Name the blood parasite species.
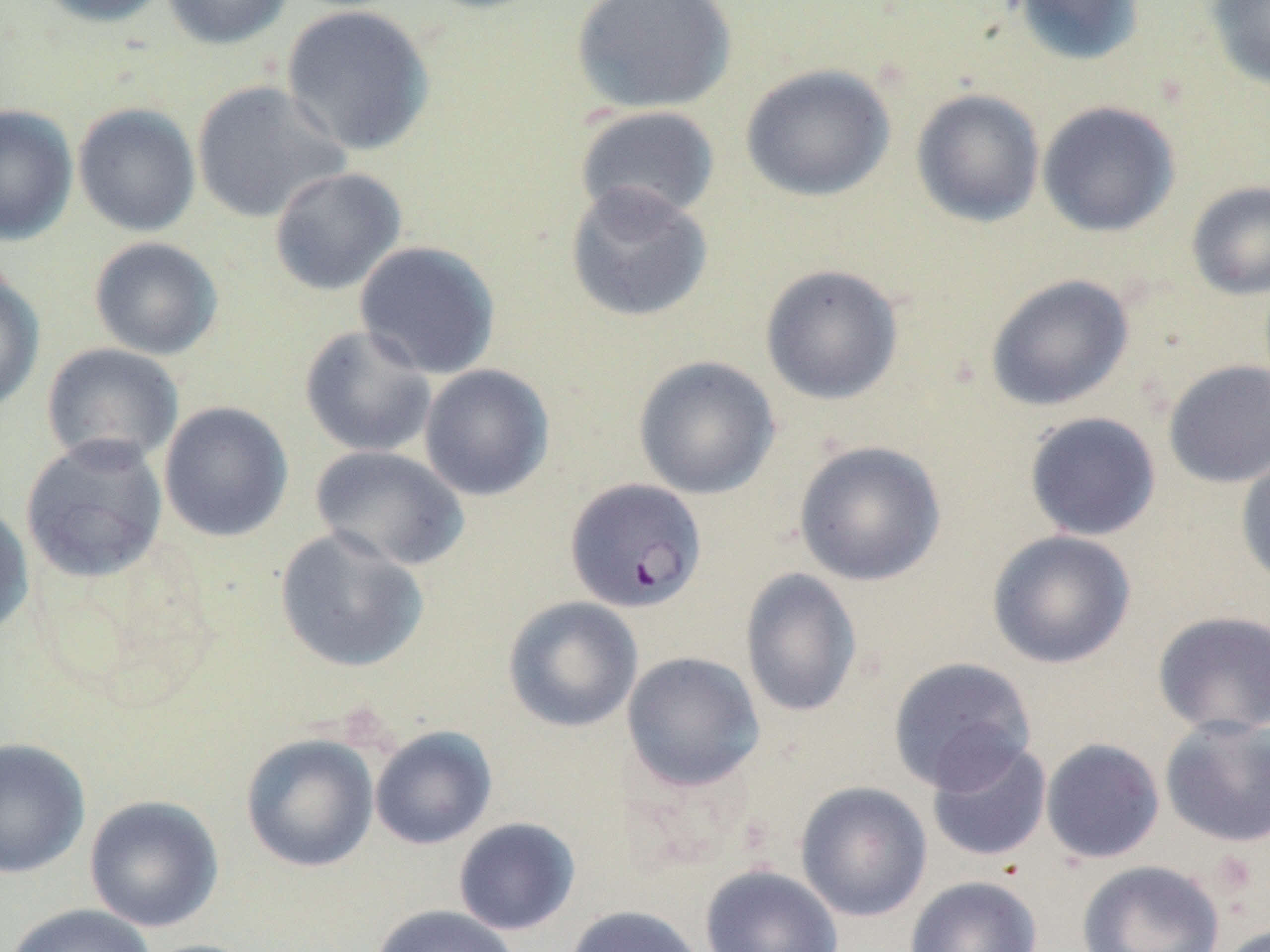

Plasmodium falciparum.

Approximate bounding boxes as (x1, y1, x2, y2) in pixels. Plasmodium falciparum-infected red blood cell locations: (565, 477, 707, 613). Uninfected red blood cell locations: (35, 0, 170, 27), (159, 0, 294, 49), (413, 0, 555, 15), (570, 0, 738, 114), (1011, 0, 1145, 67), (1205, 0, 1270, 92), (280, 4, 435, 157), (740, 63, 897, 202), (190, 80, 351, 224), (911, 88, 1045, 227), (1037, 100, 1180, 237), (73, 103, 202, 237), (0, 104, 79, 246), (574, 106, 721, 224), (269, 167, 407, 296), (1186, 180, 1270, 301), (564, 181, 714, 323), (89, 236, 224, 360), (353, 240, 502, 379), (759, 264, 904, 405), (0, 269, 45, 416), (985, 273, 1134, 412), (299, 324, 438, 458), (41, 342, 185, 470), (633, 355, 781, 499), (1162, 359, 1270, 488), (419, 364, 554, 502), (158, 401, 294, 542), (1023, 412, 1162, 541), (20, 434, 169, 584), (793, 440, 947, 586), (309, 445, 471, 572), (1235, 448, 1270, 589), (0, 501, 35, 639), (274, 527, 430, 673), (986, 529, 1136, 669), (740, 568, 864, 718), (502, 596, 643, 733), (1151, 610, 1270, 738), (621, 651, 765, 792), (888, 656, 1036, 794), (1159, 715, 1270, 848), (369, 726, 498, 850), (240, 732, 380, 873), (0, 737, 91, 879), (924, 738, 1053, 863), (1040, 738, 1165, 864), (795, 781, 933, 922), (83, 794, 225, 932), (453, 817, 581, 936), (1076, 860, 1225, 952), (700, 864, 844, 952), (904, 876, 1043, 952), (4, 903, 158, 952), (369, 904, 521, 952), (564, 904, 706, 952), (1214, 921, 1269, 952). Single field of view. Optical microscopy. Thin blood smear. Captured at 1000x magnification. Image is 1270×952 pixels. May-Grünwald-Giemsa-stained preparation.